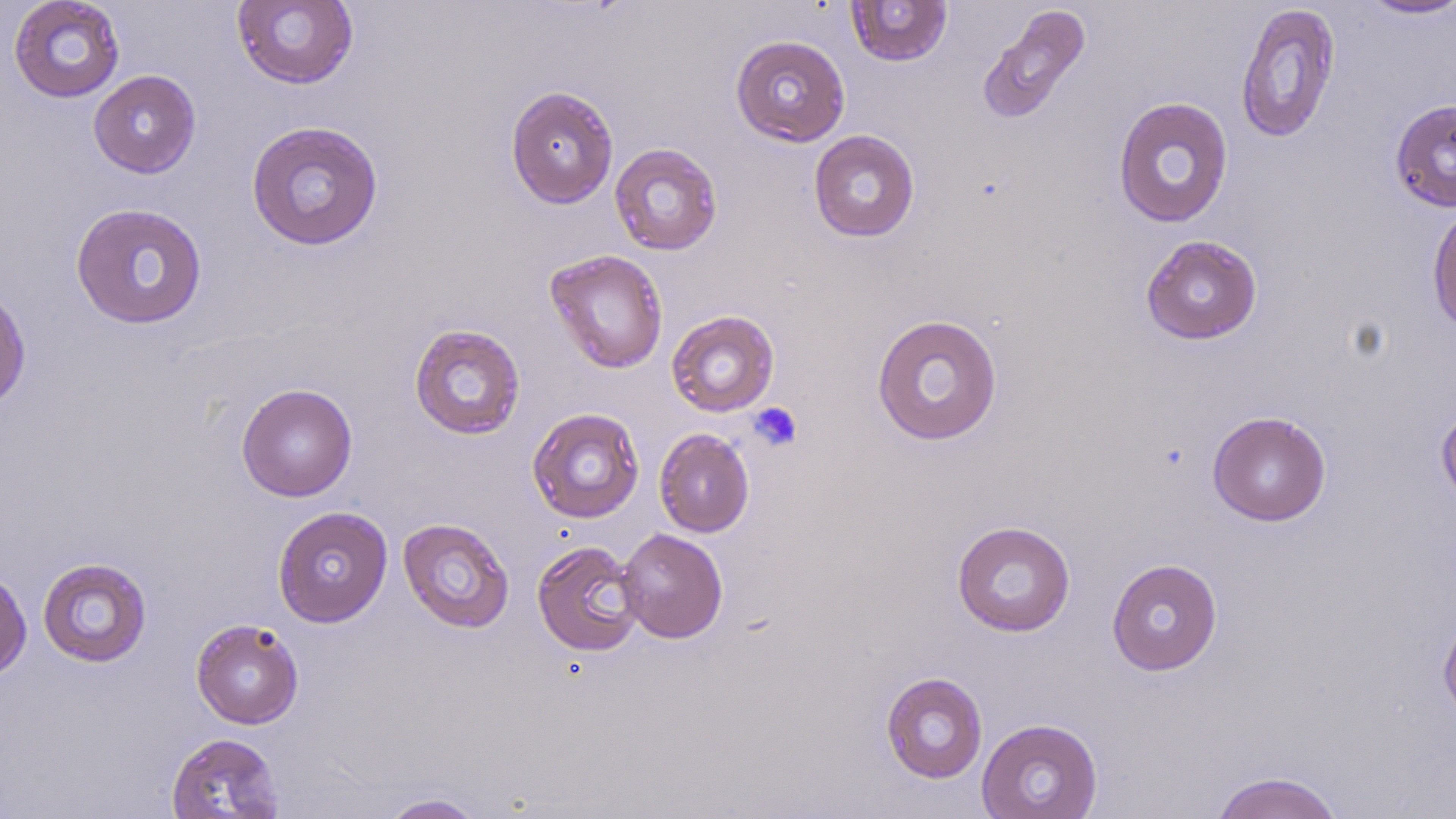
Summary:
  - Coordinate format: approximate bounding boxes as named x1/y1/x2/y2 corners in pixels
  - Uninfected red blood cell locations: (x1=8, y1=0, x2=126, y2=103), (x1=845, y1=0, x2=952, y2=67), (x1=1358, y1=0, x2=1456, y2=20), (x1=232, y1=1, x2=359, y2=90), (x1=1235, y1=3, x2=1341, y2=144), (x1=977, y1=5, x2=1091, y2=125), (x1=730, y1=34, x2=850, y2=147), (x1=88, y1=70, x2=201, y2=178), (x1=505, y1=85, x2=619, y2=209), (x1=1112, y1=96, x2=1234, y2=228), (x1=1390, y1=98, x2=1456, y2=212), (x1=246, y1=120, x2=384, y2=251), (x1=808, y1=129, x2=920, y2=242), (x1=609, y1=143, x2=723, y2=255), (x1=70, y1=202, x2=208, y2=329), (x1=1427, y1=203, x2=1456, y2=336), (x1=1140, y1=234, x2=1263, y2=344), (x1=545, y1=249, x2=669, y2=374), (x1=0, y1=286, x2=31, y2=415), (x1=666, y1=309, x2=780, y2=417), (x1=871, y1=314, x2=1003, y2=446), (x1=409, y1=323, x2=525, y2=440), (x1=236, y1=383, x2=358, y2=502), (x1=1435, y1=402, x2=1456, y2=510), (x1=527, y1=407, x2=645, y2=523), (x1=1207, y1=411, x2=1331, y2=526), (x1=654, y1=428, x2=755, y2=537), (x1=272, y1=506, x2=393, y2=627), (x1=398, y1=517, x2=515, y2=633), (x1=951, y1=520, x2=1076, y2=637), (x1=616, y1=527, x2=728, y2=643), (x1=532, y1=539, x2=644, y2=656), (x1=37, y1=557, x2=152, y2=667), (x1=1106, y1=558, x2=1223, y2=675), (x1=0, y1=569, x2=32, y2=681), (x1=1438, y1=611, x2=1456, y2=725), (x1=191, y1=618, x2=304, y2=729), (x1=880, y1=671, x2=988, y2=783), (x1=977, y1=718, x2=1104, y2=819), (x1=165, y1=732, x2=285, y2=819), (x1=1209, y1=770, x2=1346, y2=819), (x1=377, y1=793, x2=488, y2=818)
  - Platelet locations: (x1=748, y1=402, x2=802, y2=452)
  - Slide-level diagnosis: no evidence of blood parasites
  - Modality: light microscopy
  - Magnification: 1000x
  - Field of view: single
  - Image size: 1456×819 pixels
  - Preparation: thin blood smear
  - Stain: May-Grünwald-Giemsa